Locate every blood parasite and identify its species.
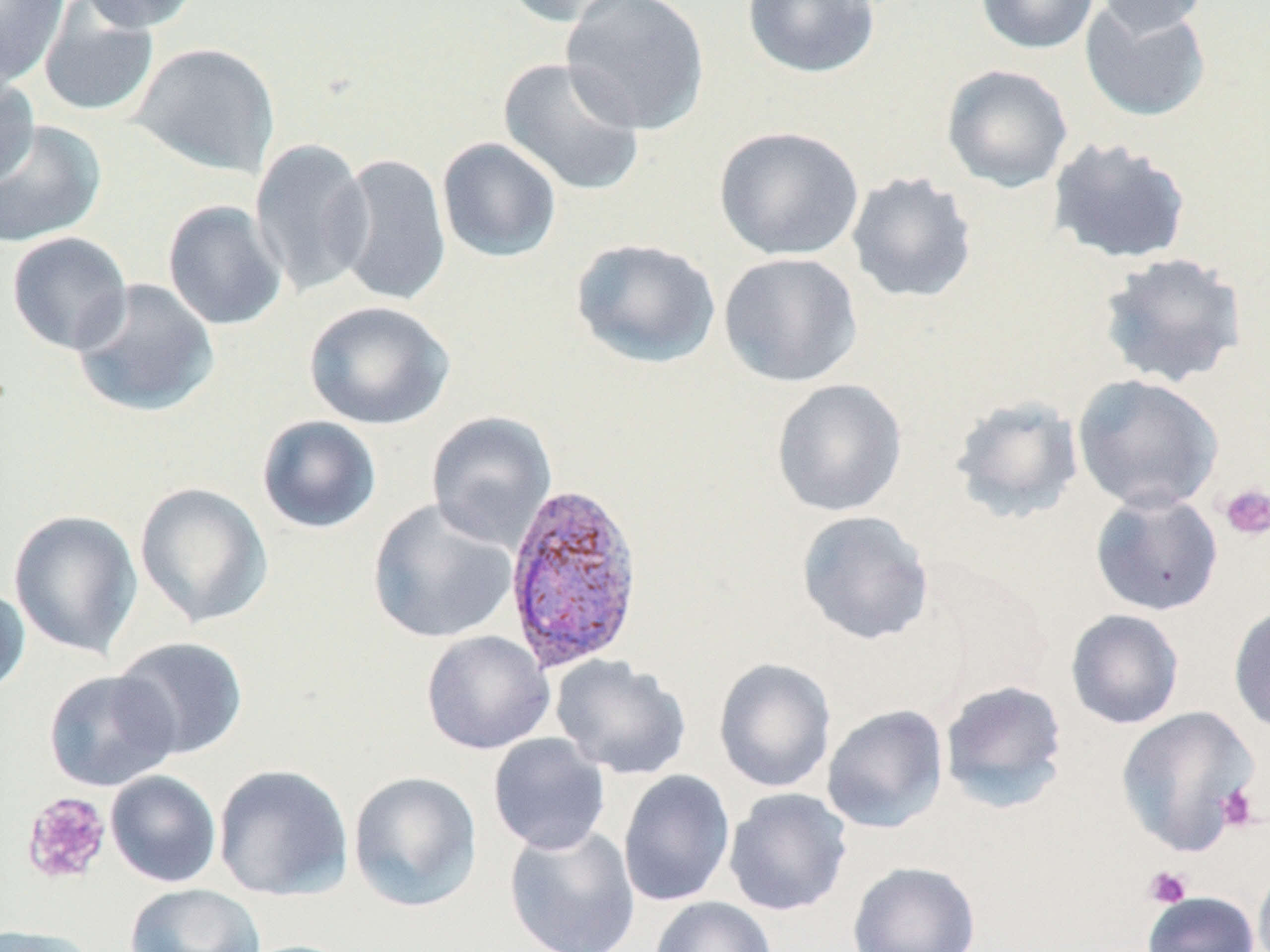
Approximate bounding boxes as (x1,y1)-(x2,y2) corner pairs in pixels.
Plasmodium vivax-infected red blood cells: (503,480)-(645,673).
No Plasmodium falciparum, Plasmodium ovale, Plasmodium malariae, Babesia divergens, or Trypanosoma brucei observed.

slide_level_diagnosis: Plasmodium vivax
stain: May-Grünwald-Giemsa
platelet_locations: 'approximate bounding boxes as (x1,y1)-(x2,y2) corner pairs in pixels: (1219,483)-(1270,541), (1217,783)-(1260,833), (20,791)-(113,886), (1143,866)-(1192,909)'
field_of_view: single
uninfected_red_blood_cell_locations: 'approximate bounding boxes as (x1,y1)-(x2,y2) corner pairs in pixels: (0,0)-(69,88), (76,0)-(201,33), (501,0)-(642,28), (560,0)-(711,135), (742,0)-(882,79), (975,0)-(1099,54), (1095,0)-(1210,37), (1079,1)-(1212,123), (38,2)-(160,119), (128,42)-(280,179), (497,55)-(646,197), (941,64)-(1074,193), (0,73)-(40,189), (0,119)-(106,249), (714,125)-(864,261), (250,137)-(374,298), (436,137)-(562,263), (1046,137)-(1193,266), (331,153)-(453,308), (846,171)-(978,304), (162,200)-(288,331), (6,231)-(133,355), (570,237)-(721,369), (1096,251)-(1248,389), (718,252)-(863,388), (71,278)-(220,418), (303,300)-(455,430), (1072,374)-(1223,513), (771,378)-(907,518), (949,394)-(1084,525), (426,411)-(557,551), (256,415)-(382,534), (133,481)-(273,630), (1089,490)-(1224,617), (367,499)-(518,644), (8,509)-(143,660), (796,510)-(934,645), (0,581)-(31,698), (1228,602)-(1270,735), (1065,609)-(1185,730), (420,630)-(555,755), (111,637)-(249,761), (551,655)-(693,780), (713,656)-(836,793), (43,669)-(180,792), (939,679)-(1069,813), (821,704)-(949,833), (1115,705)-(1259,856), (488,733)-(610,855), (213,763)-(354,901), (617,769)-(736,907), (105,770)-(222,888), (348,771)-(483,913), (723,787)-(852,916), (503,823)-(641,952), (1253,860)-(1270,952), (847,861)-(980,952), (124,883)-(266,952), (1142,891)-(1260,952), (649,896)-(777,952), (0,925)-(100,952)'
magnification: 1000x
preparation: thin blood smear
image_size: 1270×952 pixels
modality: optical microscopy